Name the blood parasite species.
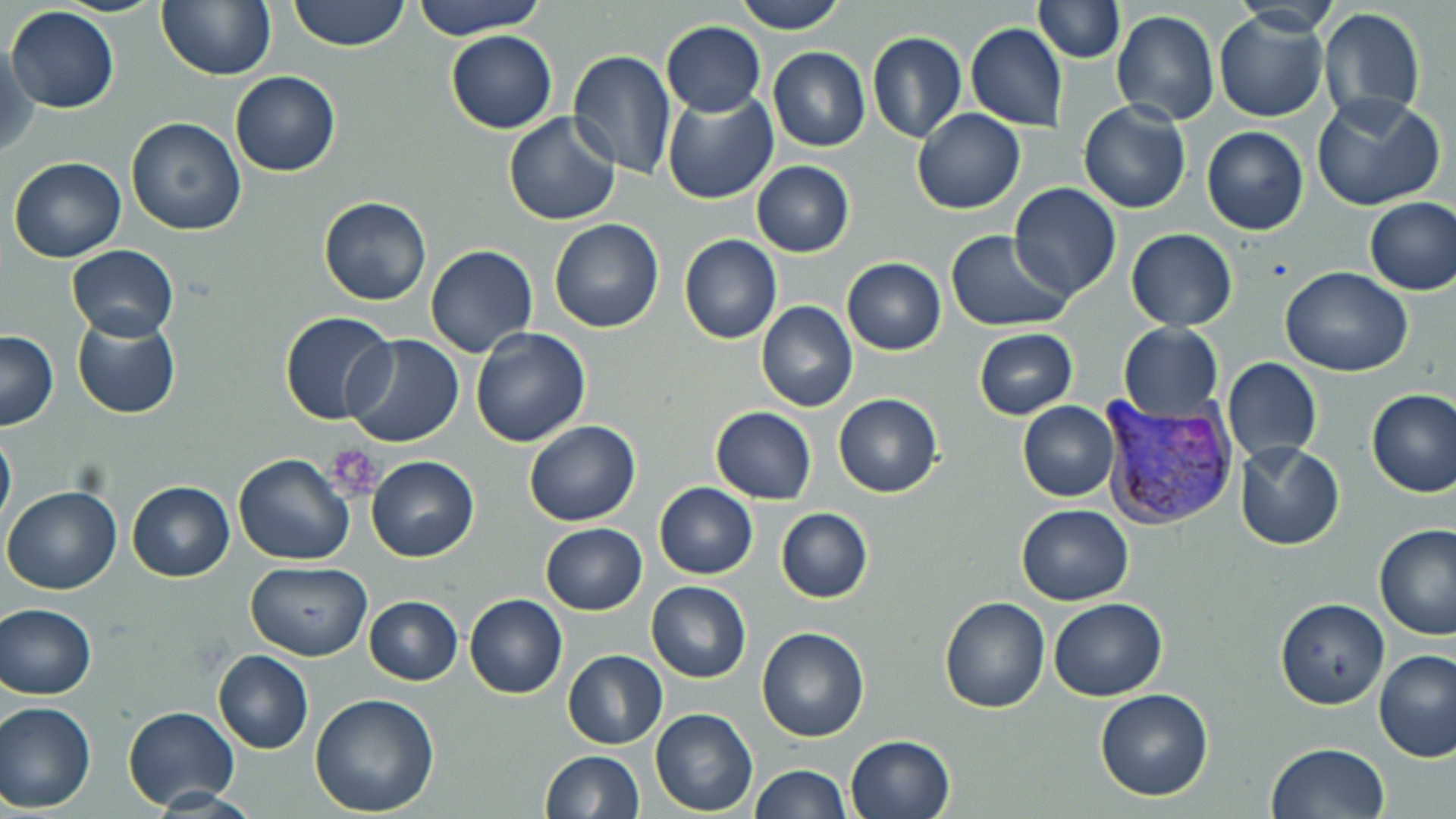
Plasmodium vivax.

Approximate bounding boxes as (x1,y1)-(x2,y2) corner pairs in pixels. Plasmodium vivax-infected red blood cell locations: (1100,394)-(1237,525). Platelet locations: (316,440)-(386,499). Uninfected red blood cell locations: (156,0)-(274,81), (288,0)-(410,52), (411,0)-(546,38), (733,0)-(848,34), (1035,1)-(1123,61), (1227,2)-(1345,35), (1317,6)-(1426,123), (5,7)-(120,112), (1112,10)-(1219,126), (1213,10)-(1328,123), (660,21)-(765,117), (966,24)-(1067,130), (445,29)-(557,134), (866,32)-(967,144), (2,39)-(38,159), (768,46)-(870,152), (566,50)-(677,180), (229,71)-(341,176), (662,90)-(777,205), (1311,92)-(1445,212), (1078,101)-(1190,216), (912,108)-(1026,214), (502,113)-(621,225), (126,118)-(245,236), (1202,126)-(1309,235), (8,156)-(127,263), (751,161)-(854,256), (1009,183)-(1122,301), (318,197)-(432,305), (1364,197)-(1456,295), (548,219)-(664,333), (1125,228)-(1237,331), (946,229)-(1074,330), (679,234)-(782,344), (68,245)-(178,342), (425,245)-(537,359), (842,257)-(946,355), (1280,267)-(1413,376), (756,302)-(857,413), (280,312)-(396,424), (71,314)-(182,419), (1118,323)-(1223,423), (470,328)-(591,448), (973,328)-(1077,419), (0,329)-(58,429), (343,333)-(465,449), (1222,358)-(1321,462), (1367,389)-(1456,497), (833,393)-(943,497), (1018,401)-(1119,501), (710,407)-(816,504), (523,421)-(641,526), (0,425)-(16,532), (1235,441)-(1343,551), (233,454)-(355,565), (367,455)-(479,562), (127,481)-(234,582), (654,483)-(757,579), (3,485)-(123,595), (1015,504)-(1134,605), (775,507)-(873,603), (540,523)-(648,614), (1373,524)-(1455,641), (245,562)-(372,660), (647,581)-(751,683), (465,593)-(567,697), (939,596)-(1049,714), (364,597)-(462,685), (1275,597)-(1389,710), (1048,598)-(1167,702), (1,603)-(97,699), (756,627)-(869,742), (1374,647)-(1456,762), (212,649)-(313,755), (563,649)-(668,750), (1095,688)-(1214,801), (309,692)-(440,815), (0,701)-(95,813), (122,706)-(239,811), (650,708)-(757,815), (844,734)-(955,819), (1266,743)-(1388,819), (539,750)-(644,819), (750,764)-(850,819). Captured at 1000x magnification. Thin blood film. May-Grünwald-Giemsa stain. Optical microscopy. Single field of view. Image is 1456×819 pixels.